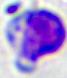

identification: white blood cell
modality: micrograph
magnification: 400x